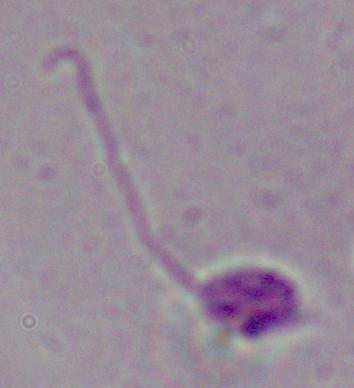

identification = Leishmania
magnification = 1000x
modality = photomicrograph